Locate every Plasmodium parasite.
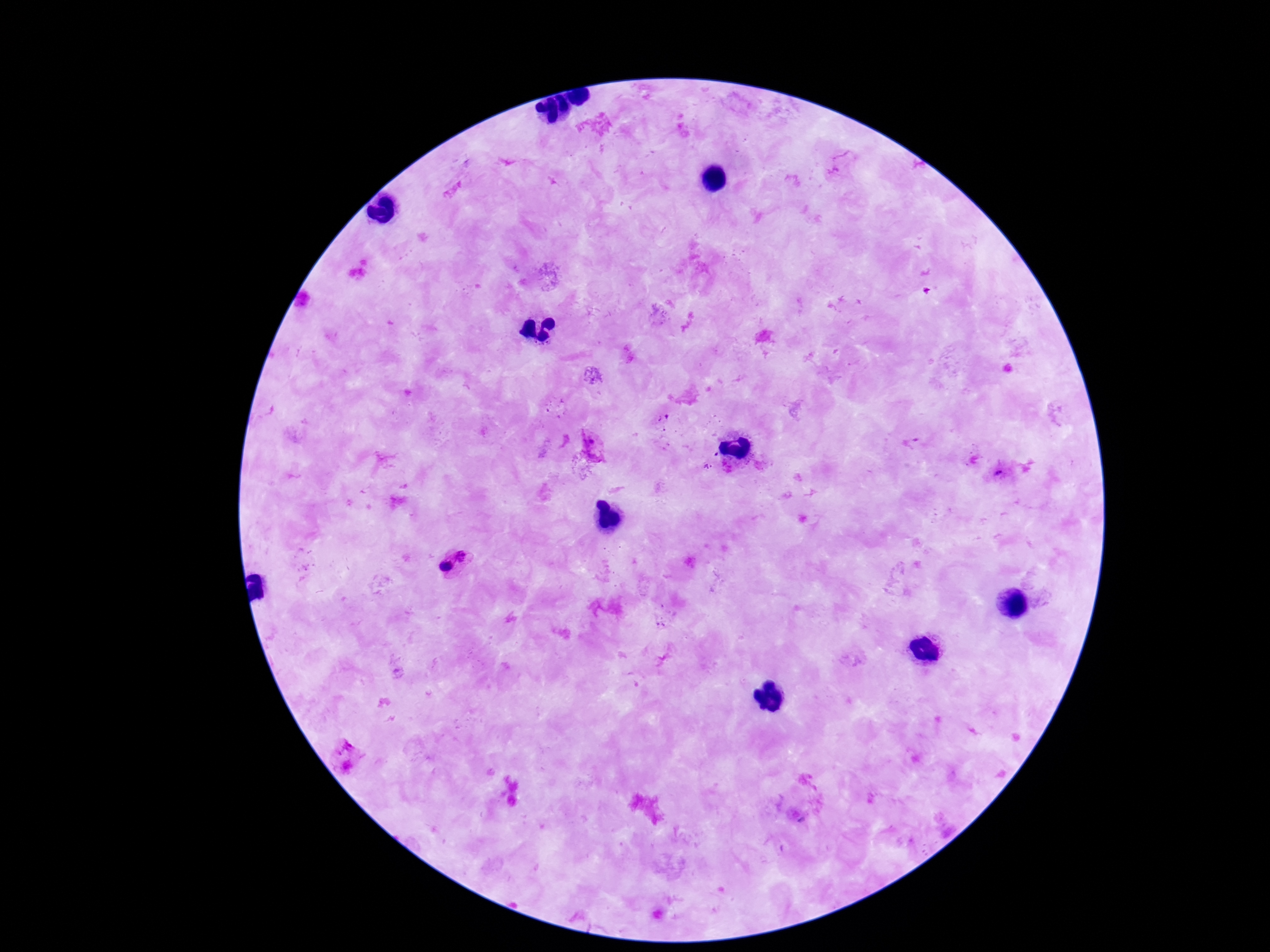

Approximate centers as (x, y) in pixels.
Plasmodium parasites: (842, 163), (594, 445), (999, 473), (466, 555), (447, 569), (344, 744), (347, 767).

Summary:
  - Preparation: thick peripheral-blood smear
  - Capture: smartphone camera through the microscope eyepiece
  - Field of view: one from this slide
  - Patient malaria status: positive
  - Magnification: 100x
  - Stain: Giemsa
  - Image size: 1270×952 pixels